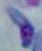 Toxoplasma gondii is shown. Photomicrograph. 1000x magnification.